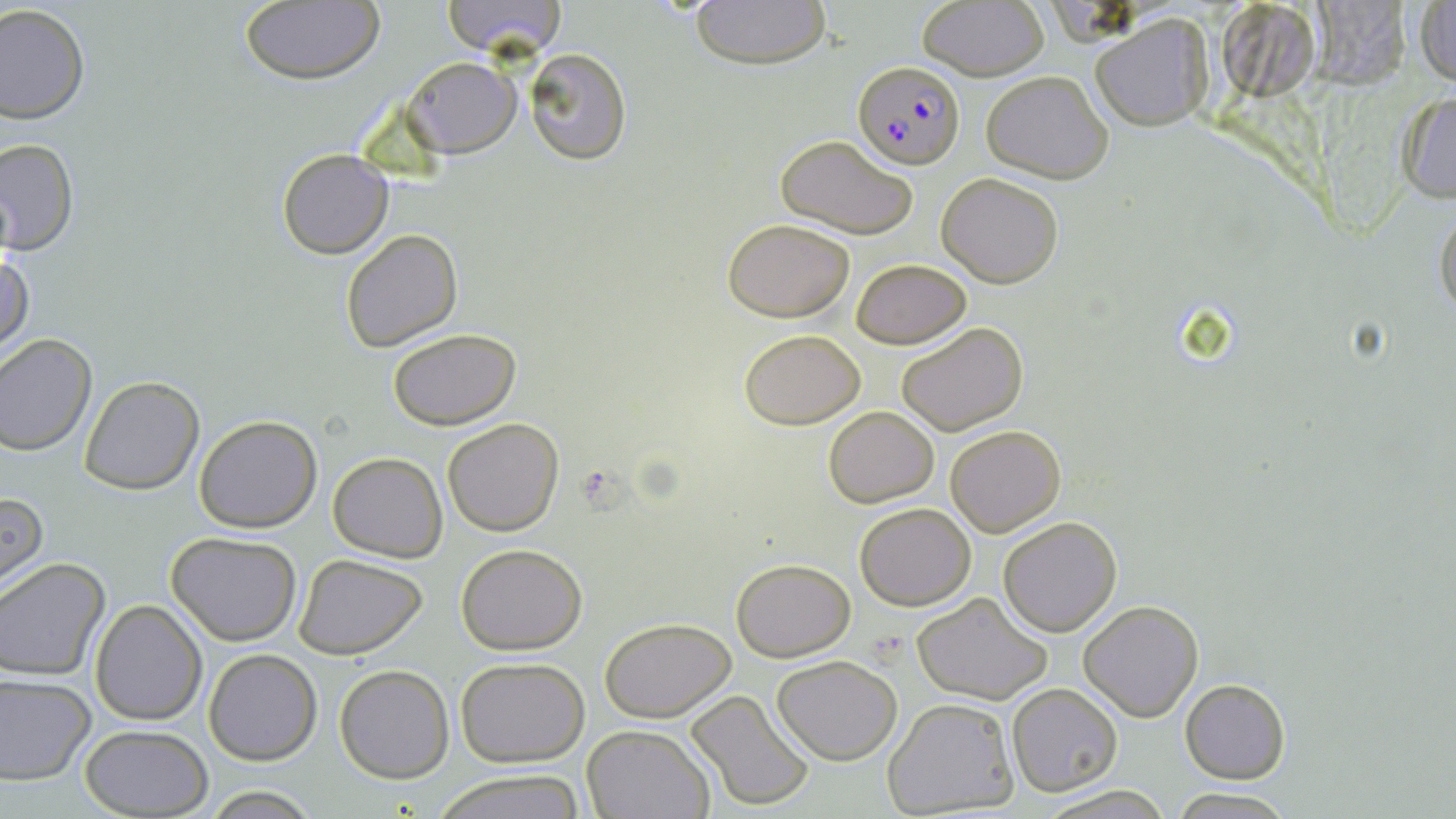

slide-level diagnosis = Plasmodium falciparum
preparation = thin blood smear
uninfected red blood cell locations = approximate bounding boxes as [x1, y1, x2, y2] in pixels: [439, 0, 568, 59], [687, 0, 831, 70], [915, 1, 1049, 81], [237, 2, 385, 85], [1414, 3, 1455, 88], [0, 4, 89, 124], [1091, 13, 1213, 132], [523, 47, 631, 165], [404, 56, 519, 157], [981, 70, 1114, 183], [1396, 90, 1456, 203], [774, 133, 921, 239], [0, 136, 78, 256], [277, 148, 393, 258], [937, 172, 1063, 288], [1435, 204, 1456, 321], [722, 217, 855, 321], [341, 228, 462, 352], [1, 251, 35, 359], [851, 257, 971, 349], [897, 320, 1029, 438], [739, 328, 866, 430], [389, 329, 522, 430], [0, 333, 99, 455], [78, 374, 204, 495], [823, 405, 939, 508], [193, 415, 322, 533], [442, 418, 564, 536], [945, 424, 1066, 537], [328, 452, 447, 562], [0, 489, 47, 595], [854, 501, 976, 610], [997, 516, 1122, 638], [166, 531, 302, 645], [456, 542, 587, 655], [293, 552, 431, 660], [731, 557, 854, 660], [0, 559, 110, 681], [912, 592, 1052, 706], [90, 600, 207, 726], [1079, 601, 1202, 720], [600, 617, 736, 722], [203, 648, 323, 766], [772, 655, 903, 765], [456, 657, 589, 767], [334, 664, 454, 783], [0, 673, 96, 784], [1179, 679, 1290, 784], [1007, 683, 1123, 797], [686, 690, 816, 812], [883, 697, 1019, 816], [79, 723, 212, 817], [582, 723, 714, 818], [432, 769, 586, 819], [1033, 786, 1174, 818], [1168, 790, 1294, 819]
stain = May-Grünwald-Giemsa
field of view = one of a larger specimen
modality = optical microscopy
Plasmodium falciparum-infected red blood cell locations = approximate bounding boxes as [x1, y1, x2, y2] in pixels: [853, 60, 969, 171]
image size = 1456×819 pixels
magnification = 1000x